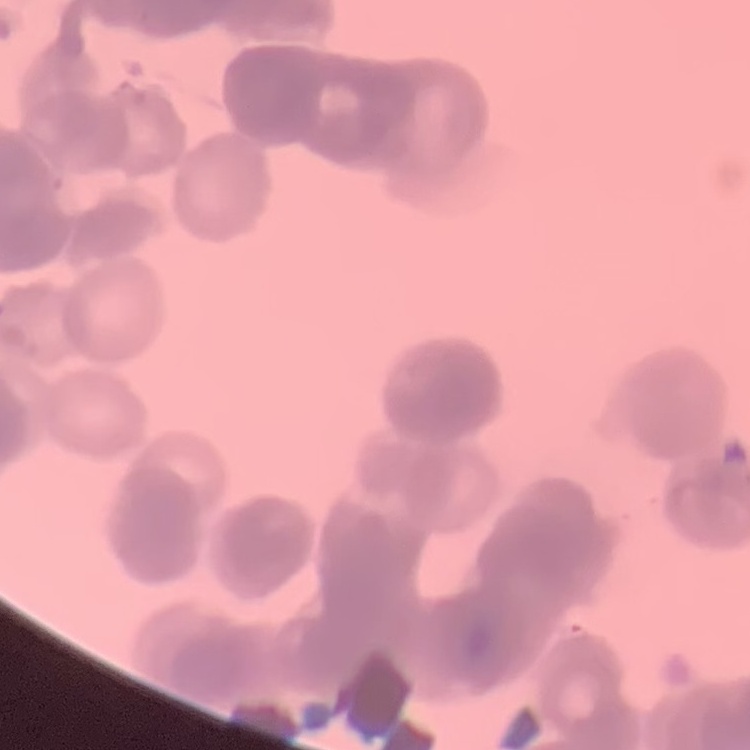
The red blood cells exhibit rouleaux formation. Thin peripheral smear. Field's or Giemsa stain. Square crop of a larger photomicrograph.